Give the position of every Plasmodium parasite, noting whether each is a trophozoite, schizont, or gametocyte.
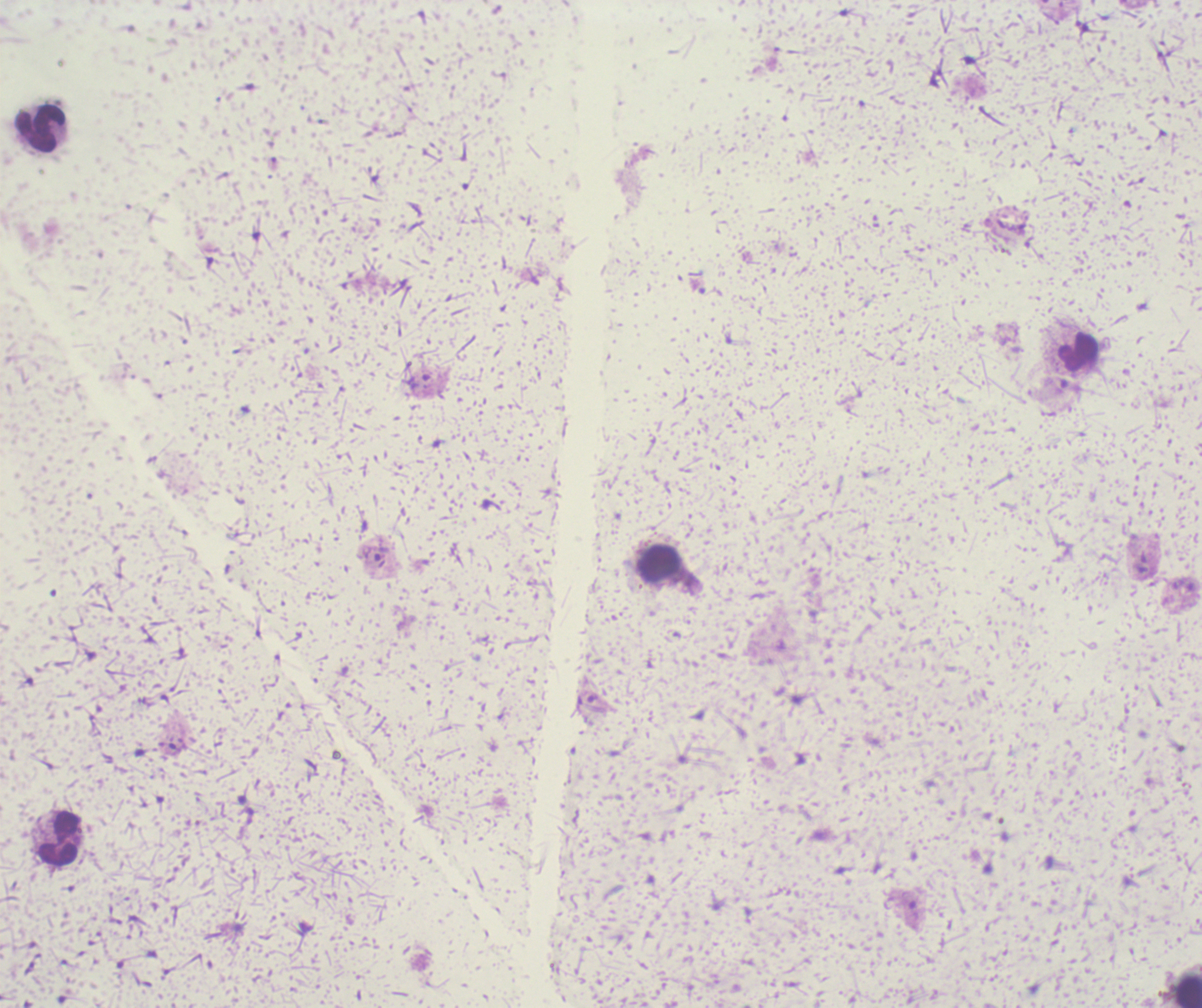
Approximate centers as [x, y] in pixels.
Trophozoites: [381, 554].
No schizont or gametocyte forms observed.

Approximate centers as [x, y] in pixels.
Summary:
  - Leukocyte locations: [39, 129], [1079, 351], [658, 561], [58, 839], [1188, 990]
  - Stain: Romanowsky
  - Background quality: unsatisfactory
  - Magnification: 100x
  - Image size: 1202×1008 pixels
  - Preparation: thick smear of blood
  - Field of view: single
  - Context: previously used in a real diagnosis